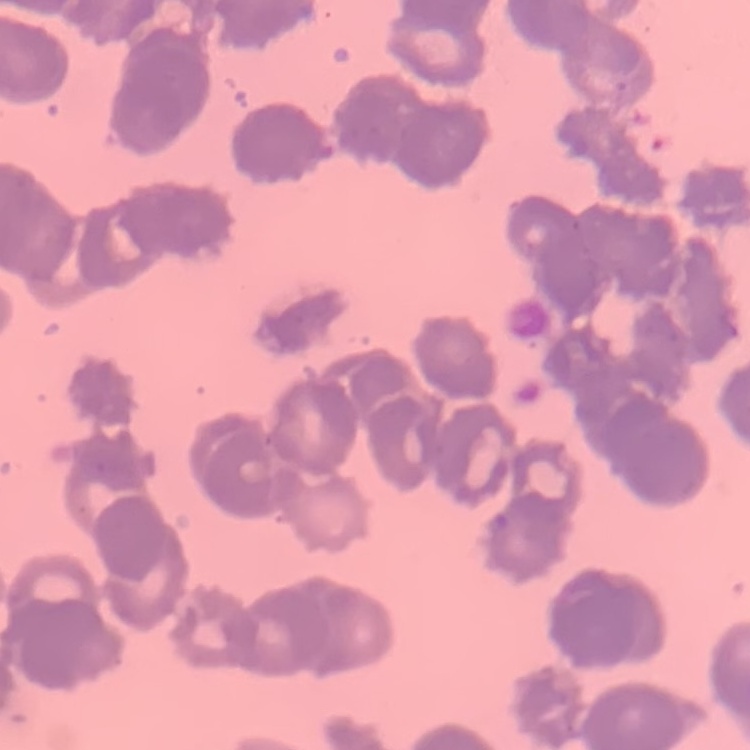
erythrocyte_morphology: rouleaux formation
image_type: one tile cut from a larger photomicrograph
stain: Field's or Giemsa
preparation: thin blood film